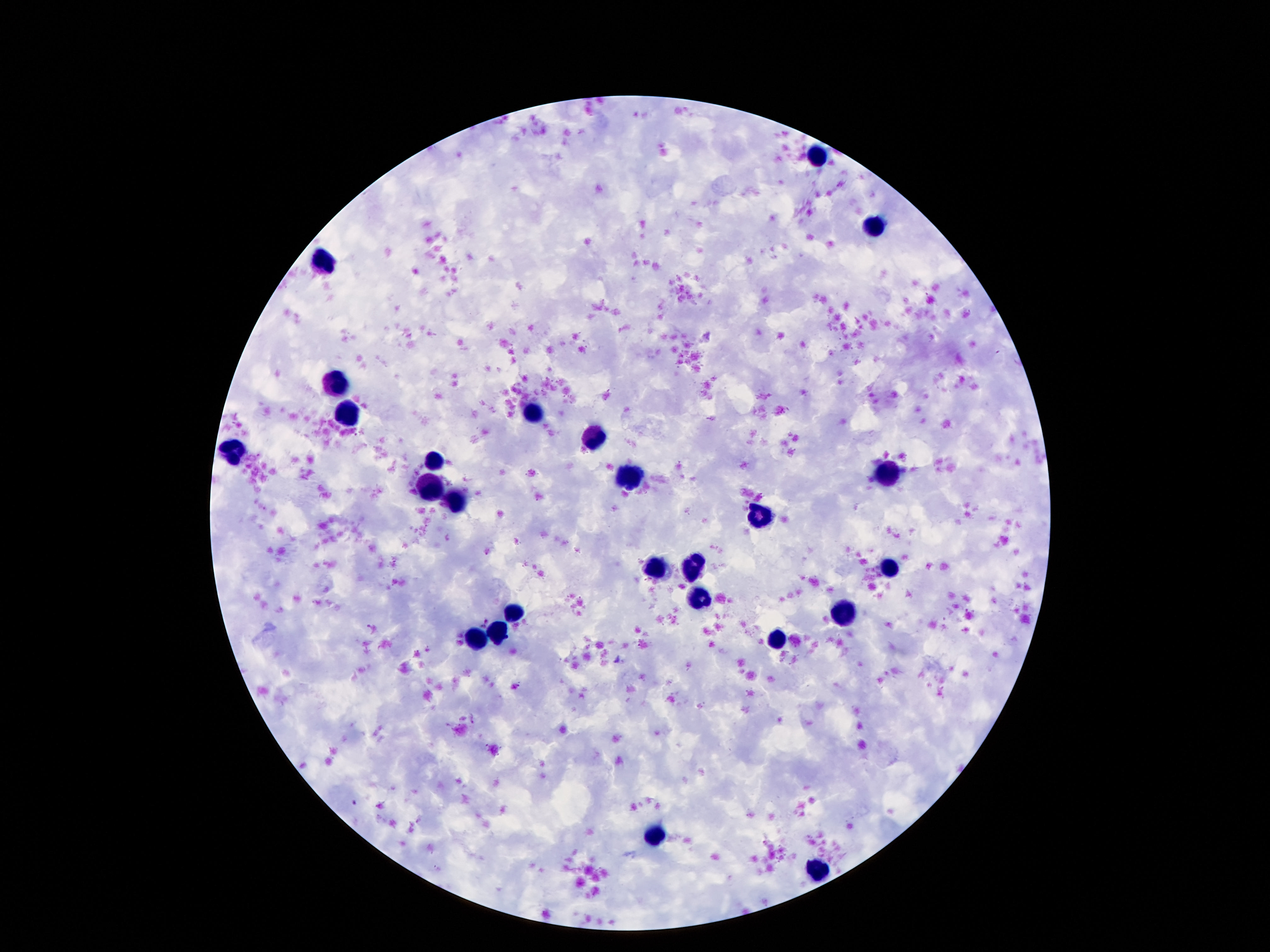
patient malaria status = negative
field of view = one from this slide
preparation = thick blood film
capture = smartphone camera through the microscope eyepiece
magnification = 100x
image size = 1270×952 pixels
stain = Giemsa
leukocyte locations = approximate object centers, in pixels from the top-left corner: (x=817, y=157), (x=874, y=226), (x=324, y=260), (x=336, y=386), (x=533, y=415), (x=345, y=416), (x=592, y=437), (x=238, y=447), (x=434, y=459), (x=889, y=473), (x=631, y=479), (x=431, y=490), (x=458, y=499), (x=758, y=518), (x=658, y=568), (x=692, y=568), (x=887, y=570), (x=697, y=597), (x=515, y=609), (x=844, y=613), (x=499, y=634), (x=477, y=638), (x=780, y=640), (x=656, y=836), (x=819, y=868)